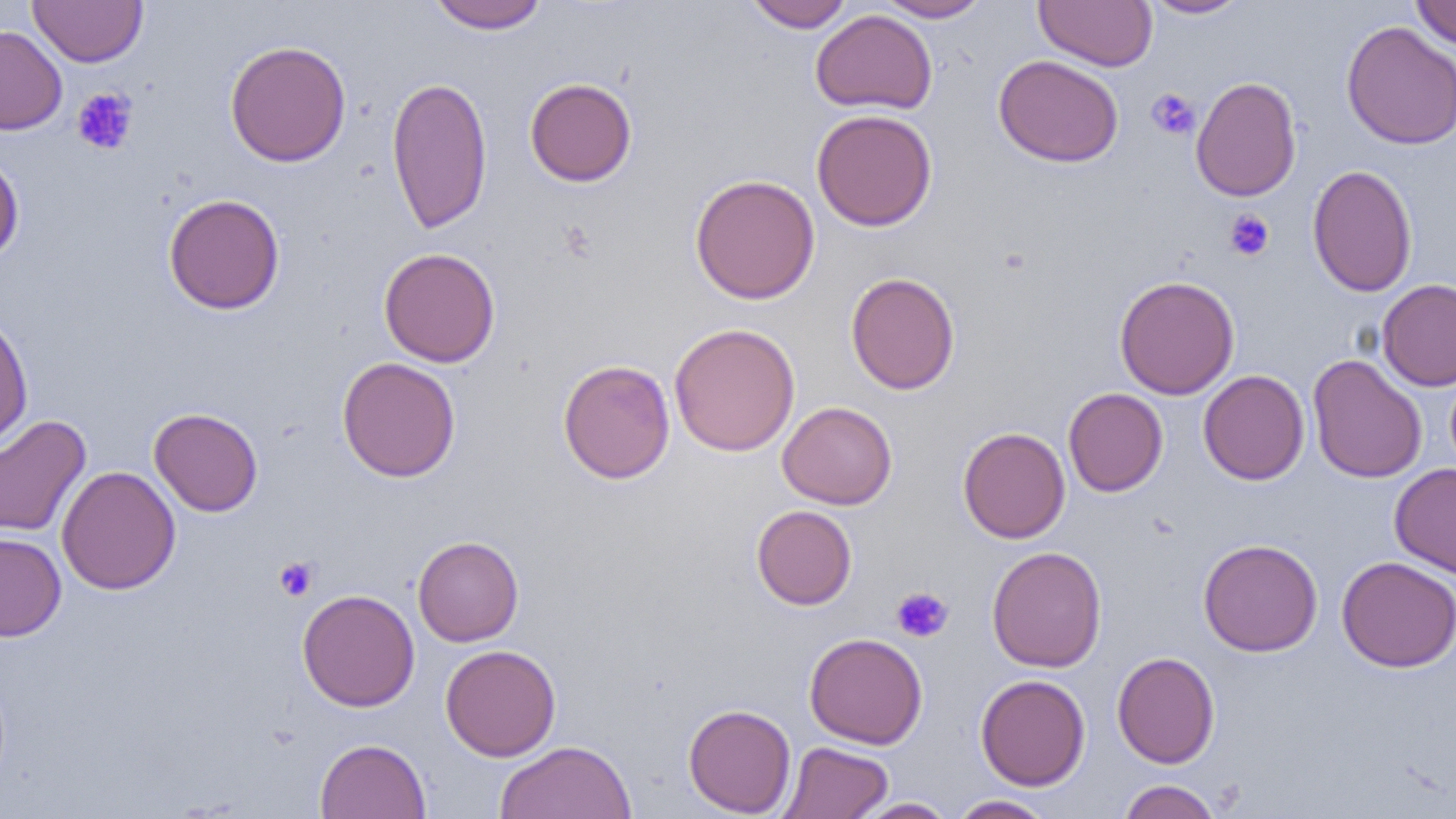

Summary:
  - Coordinate format: approximate bounding boxes as (x1,y1)-(x2,y2) corner pairs in pixels
  - Uninfected red blood cell locations: (28,0)-(148,67), (426,0)-(549,34), (743,0)-(855,32), (875,0)-(991,22), (1034,0)-(1157,71), (1140,0)-(1251,19), (1411,0)-(1456,50), (810,10)-(938,114), (1340,21)-(1456,150), (0,25)-(67,135), (224,40)-(351,167), (994,54)-(1123,168), (1190,75)-(1302,202), (386,76)-(493,234), (524,77)-(637,187), (811,109)-(938,232), (0,151)-(24,266), (1306,164)-(1418,297), (689,173)-(820,304), (163,193)-(285,315), (378,247)-(501,367), (845,272)-(960,395), (1114,275)-(1240,400), (1376,279)-(1456,392), (0,311)-(33,450), (669,323)-(801,457), (1307,354)-(1427,484), (337,356)-(461,482), (558,359)-(675,484), (1198,369)-(1310,485), (1063,388)-(1168,496), (777,401)-(897,509), (149,408)-(263,516), (0,414)-(91,537), (957,427)-(1070,544), (1389,463)-(1456,578), (56,465)-(181,595), (751,505)-(857,610), (0,532)-(66,642), (413,535)-(524,646), (1198,538)-(1323,657), (986,546)-(1107,672), (1336,556)-(1456,672), (297,589)-(420,712), (804,632)-(928,749), (440,644)-(561,761), (1112,651)-(1220,768), (976,673)-(1091,790), (683,703)-(797,817), (315,738)-(431,819), (494,740)-(636,819), (778,741)-(893,818), (1116,779)-(1222,819), (947,795)-(1057,818), (851,798)-(956,818)
  - Platelet locations: (71,88)-(138,155), (1146,89)-(1200,140), (1224,210)-(1275,261), (274,557)-(318,601), (891,587)-(953,642)
  - Slide-level diagnosis: negative for blood parasites
  - Preparation: thin blood smear
  - Image size: 1456×819 pixels
  - Modality: optical microscopy
  - Field of view: single
  - Magnification: 1000x